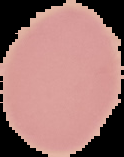
preparation = thin blood film
image type = segmented cell region on a black background
result = no malaria parasites seen
image size = 124×157 pixels